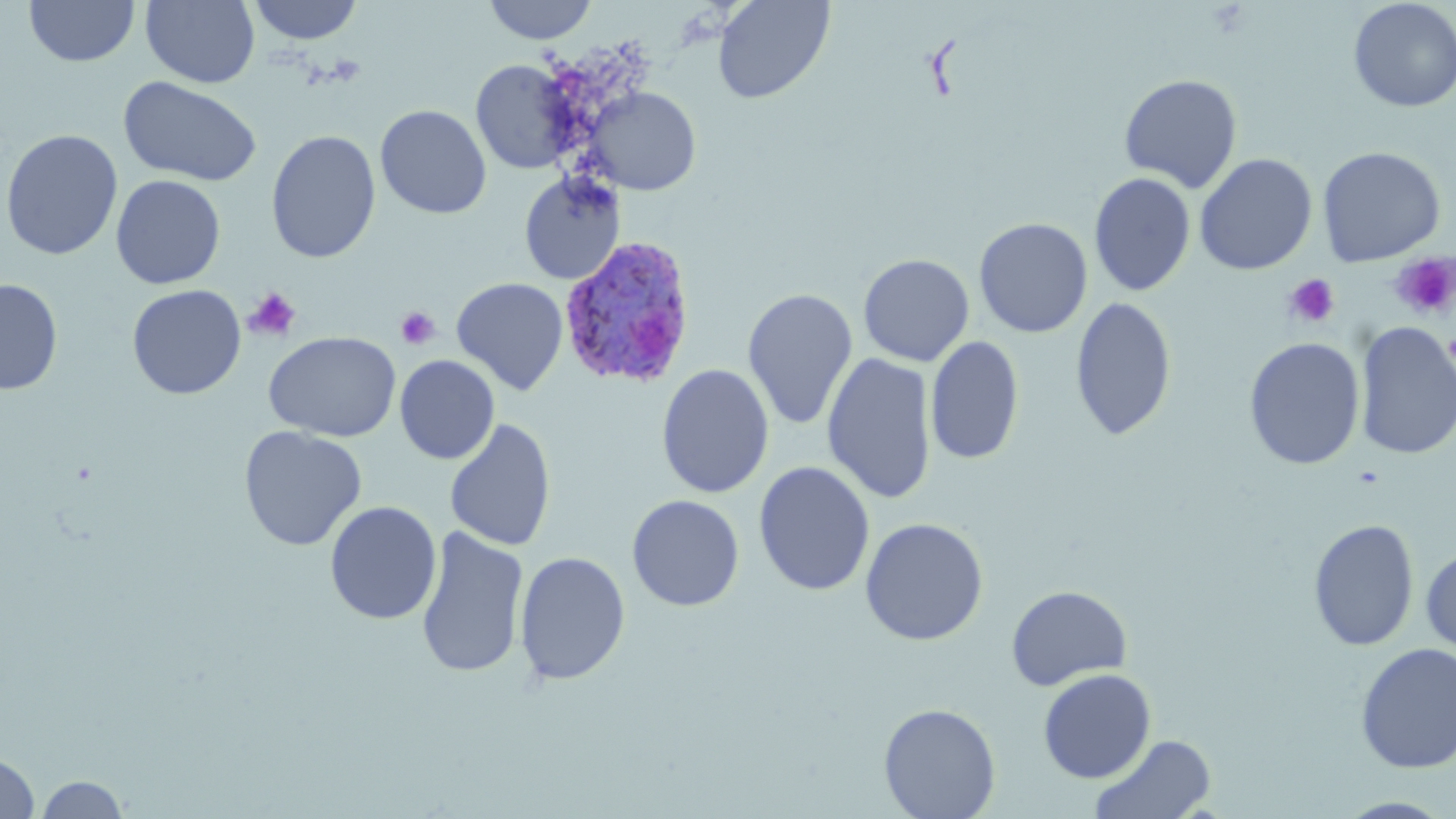 Approximate bounding boxes as (x1,y1)-(x2,y2) corner pairs in pixels. Uninfected red blood cell locations: (24,0)-(140,67), (141,0)-(260,88), (248,0)-(364,45), (483,0)-(598,44), (712,0)-(834,104), (1347,0)-(1456,113), (471,59)-(580,175), (1118,74)-(1243,193), (119,76)-(263,187), (585,86)-(701,195), (374,104)-(492,219), (1,129)-(123,260), (266,130)-(381,263), (1316,146)-(1446,267), (1194,153)-(1317,275), (519,171)-(625,285), (1089,171)-(1196,297), (110,174)-(226,289), (973,217)-(1092,338), (858,253)-(975,366), (451,276)-(569,396), (0,279)-(63,395), (127,284)-(246,400), (742,287)-(858,431), (1070,296)-(1177,441), (1354,323)-(1456,460), (263,331)-(401,442), (925,336)-(1024,466), (1244,337)-(1364,470), (822,353)-(937,505), (395,355)-(499,465), (656,363)-(774,499), (444,418)-(556,552), (239,426)-(367,551), (753,460)-(875,597), (626,494)-(745,612), (324,500)-(442,625), (860,517)-(989,646), (1308,518)-(1419,652), (415,526)-(529,680), (1421,545)-(1456,656), (514,551)-(631,686), (1006,585)-(1132,691), (1354,642)-(1456,774), (1037,668)-(1156,783), (878,702)-(1001,819), (1089,733)-(1217,819), (0,752)-(41,818), (33,774)-(131,818), (1334,797)-(1454,818). Plasmodium ovale-infected red blood cell locations: (559,235)-(698,390). Platelet locations: (1390,252)-(1456,320), (1283,273)-(1340,328), (243,287)-(302,342), (395,306)-(441,350). Slide-level diagnosis: Plasmodium ovale. Single field of view. Captured at 1000x magnification. May-Grünwald-Giemsa stain. Thin blood film. Optical microscopy. Image is 1456×819 pixels.